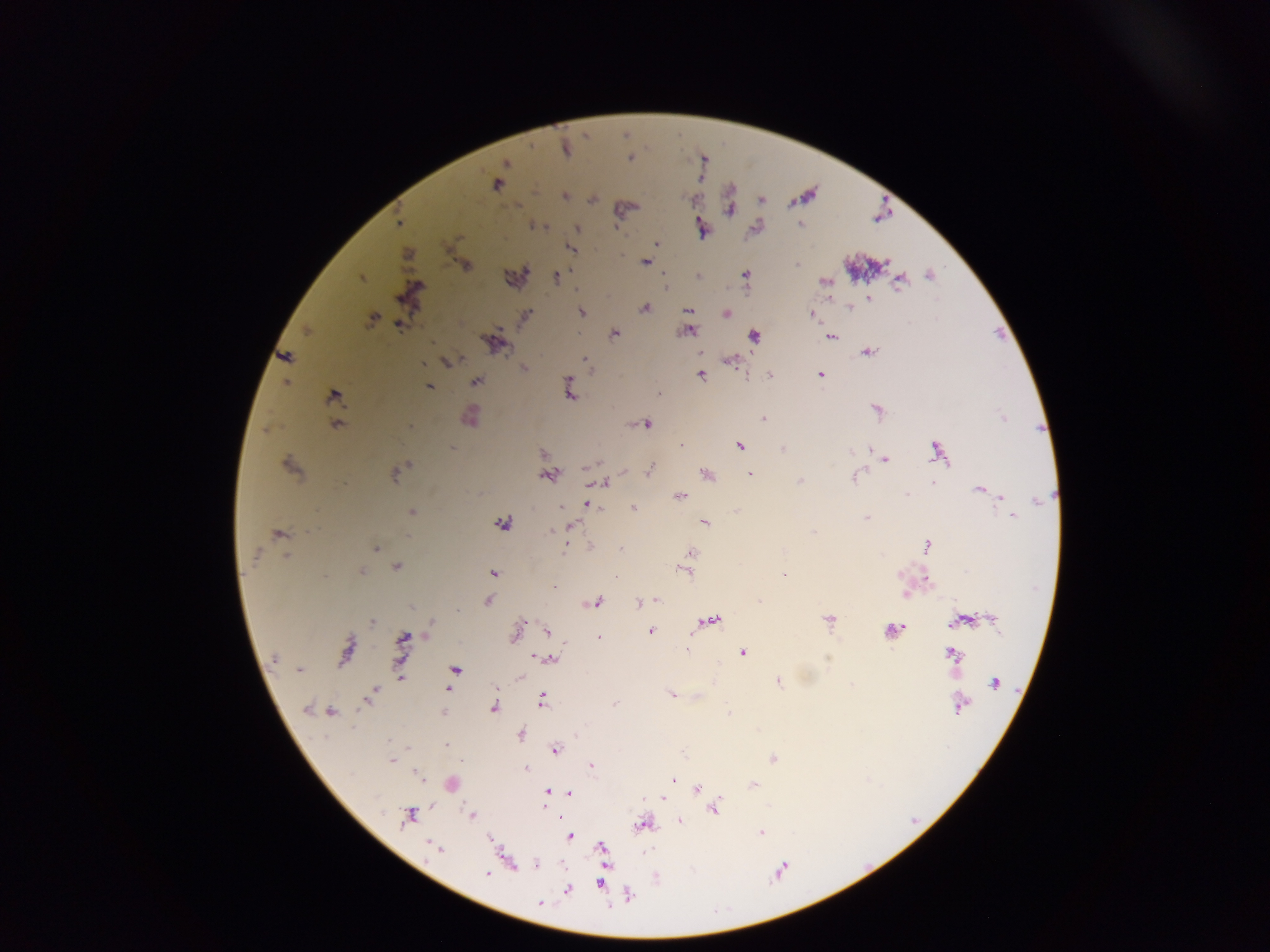 Approximate centers as x y in pixels. Plasmodium parasite locations: 565 148; 505 163; 497 184; 565 196; 592 198; 761 200; 729 210; 398 222; 801 224; 535 226; 576 227; 755 227; 701 229; 656 243; 571 248; 407 254; 645 262; 796 264; 464 266; 746 274; 517 275; 697 275; 930 275; 555 276; 361 277; 824 281; 899 281; 665 286; 411 292; 828 298; 869 298; 850 307; 645 308; 688 310; 581 311; 725 313; 812 314; 525 315; 372 318; 404 319; 399 324; 688 329; 306 330; 614 333; 753 336; 830 337; 492 344; 700 351; 868 352; 285 356; 584 359; 730 360; 447 362; 422 363; 524 368; 700 374; 769 375; 819 375; 475 381; 286 383; 429 387; 568 388; 658 393; 333 395; 876 410; 470 416; 762 418; 336 424; 644 424; 408 425; 267 429; 739 445; 680 446; 869 448; 782 450; 937 450; 885 459; 289 465; 649 469; 395 472; 706 474; 750 474; 548 475; 855 477; 799 481; 602 482; 932 483; 979 488; 679 496; 907 496; 1000 497; 587 505; 632 508; 412 512; 1012 515; 867 518; 704 522; 501 523; 569 526; 551 529; 278 534; 566 544; 927 545; 375 549; 622 549; 691 553; 286 556; 396 565; 685 570; 360 571; 493 573; 783 574; 925 578; 905 593; 655 599; 759 599; 487 601; 595 603; 639 603; 710 619; 829 619; 991 619; 372 620; 962 620; 429 627; 891 630; 515 631; 547 631; 651 631; 402 638; 598 638; 687 649; 346 650; 743 653; 951 654; 538 656; 551 658; 274 659; 455 669; 299 670; 400 677; 519 678; 778 680; 995 682; 374 687; 449 688; 372 693; 671 693; 542 700; 615 702; 960 703; 307 708; 493 708; 443 710; 330 712; 520 734; 447 743; 554 749; 772 758; 392 759; 592 765; 525 768; 417 774; 672 779; 450 783; 753 785; 696 789; 547 792; 569 793; 663 797; 643 798; 713 808; 409 815; 472 815; 559 816; 678 819; 644 824; 760 833; 568 836; 490 839; 601 847; 436 849; 509 861; 536 865; 488 873; 598 884; 567 889; 627 895; 540 903. Thick blood film. Collected in Ghana. Mobile-phone photograph taken through the microscope. One field of view. Image is 1270×952 pixels.